Give the preparation type.
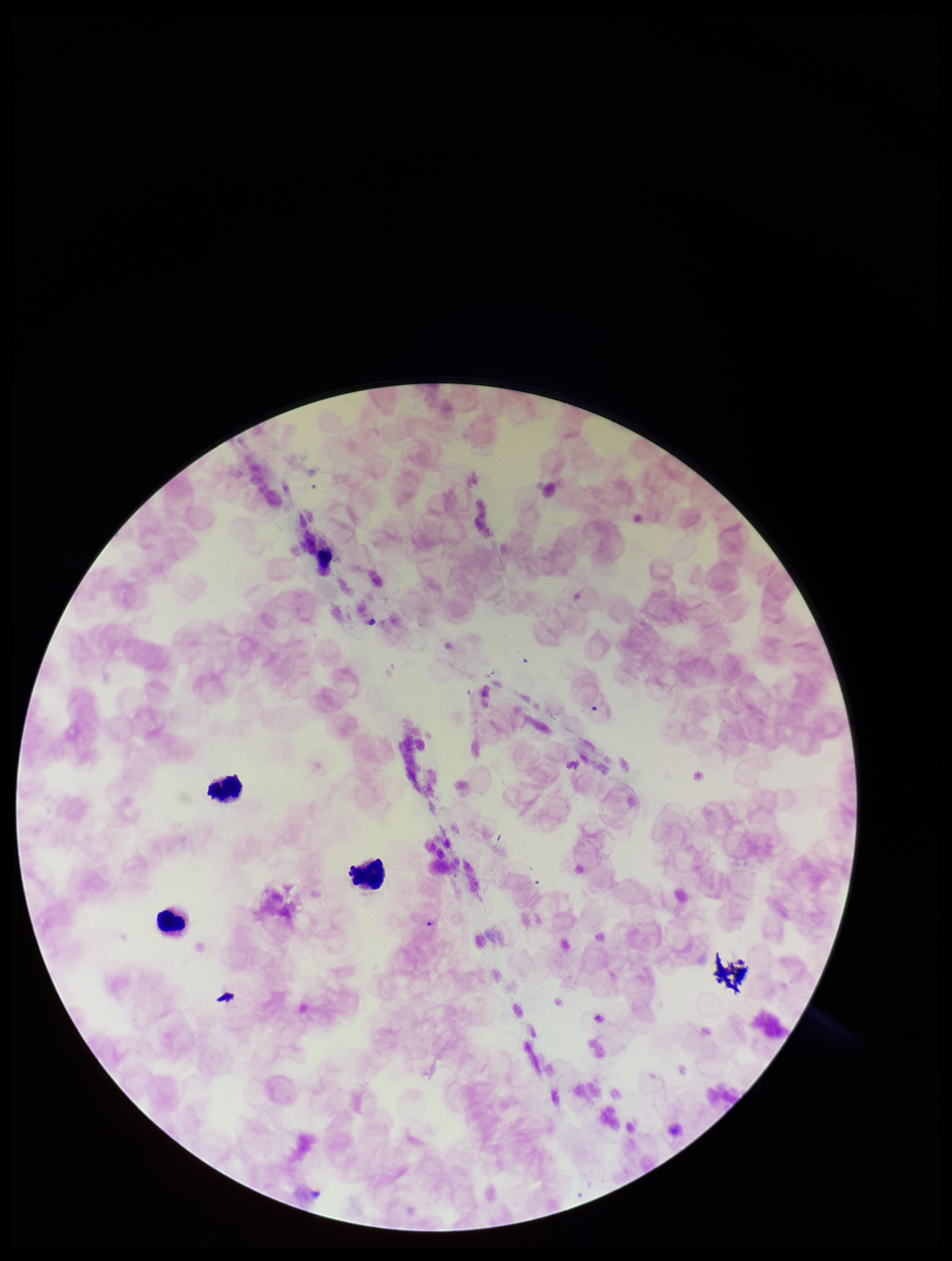

A thick smear.

Single field of view. Species reported for this patient: Plasmodium falciparum. Photographed through the microscope eyepiece with a smartphone camera. Patient malaria status: positive. Stained with Giemsa. Image is 952×1261 pixels. Leukocyte count: 3. Parasite count: 1. Plasmodium parasites: seen.